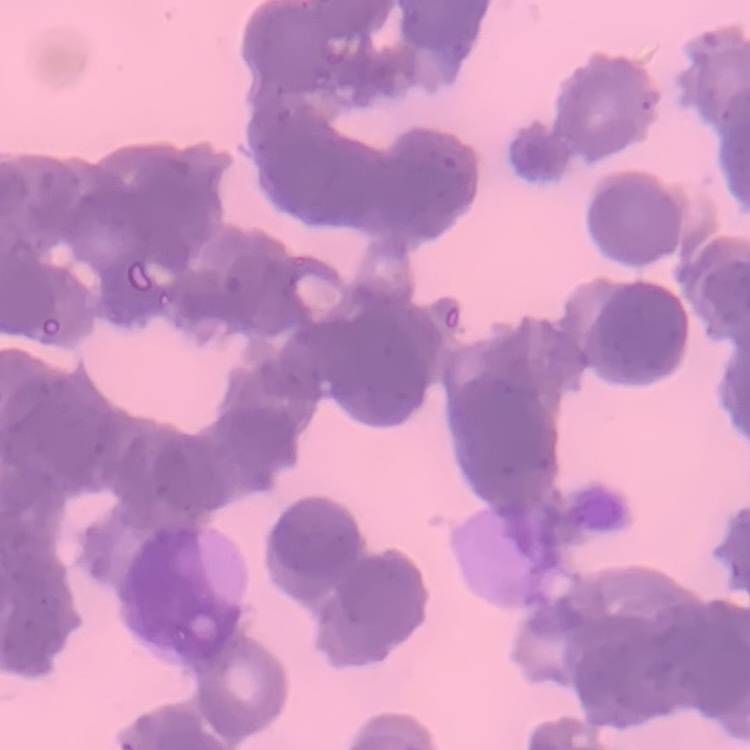

erythrocyte morphology = rouleaux formation
image type = one tile cut from a larger photomicrograph
stain = Field's or Giemsa
preparation = thin blood smear